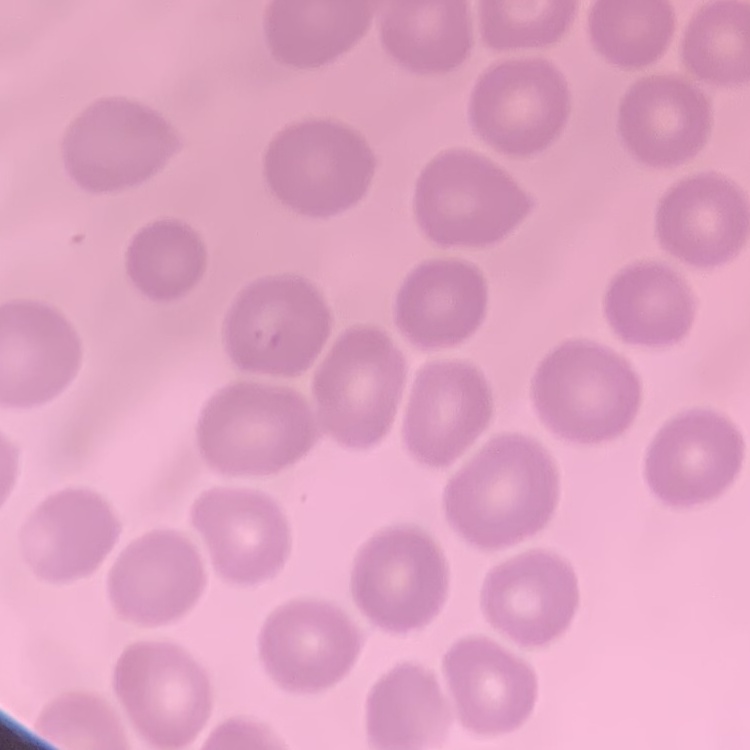
Summary:
  - Erythrocyte morphology: no rouleaux formation
  - Image type: square crop of a larger photomicrograph
  - Stain: Field's or Giemsa
  - Preparation: thin blood smear